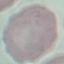

Malaria status: uninfected. Cell patch, automatically extracted from a larger field of view and resized to 64 × 64 pixels. Acquired by smartphone through the microscope eyepiece. Thin blood film. Giemsa-stained preparation.